Assess for malaria.
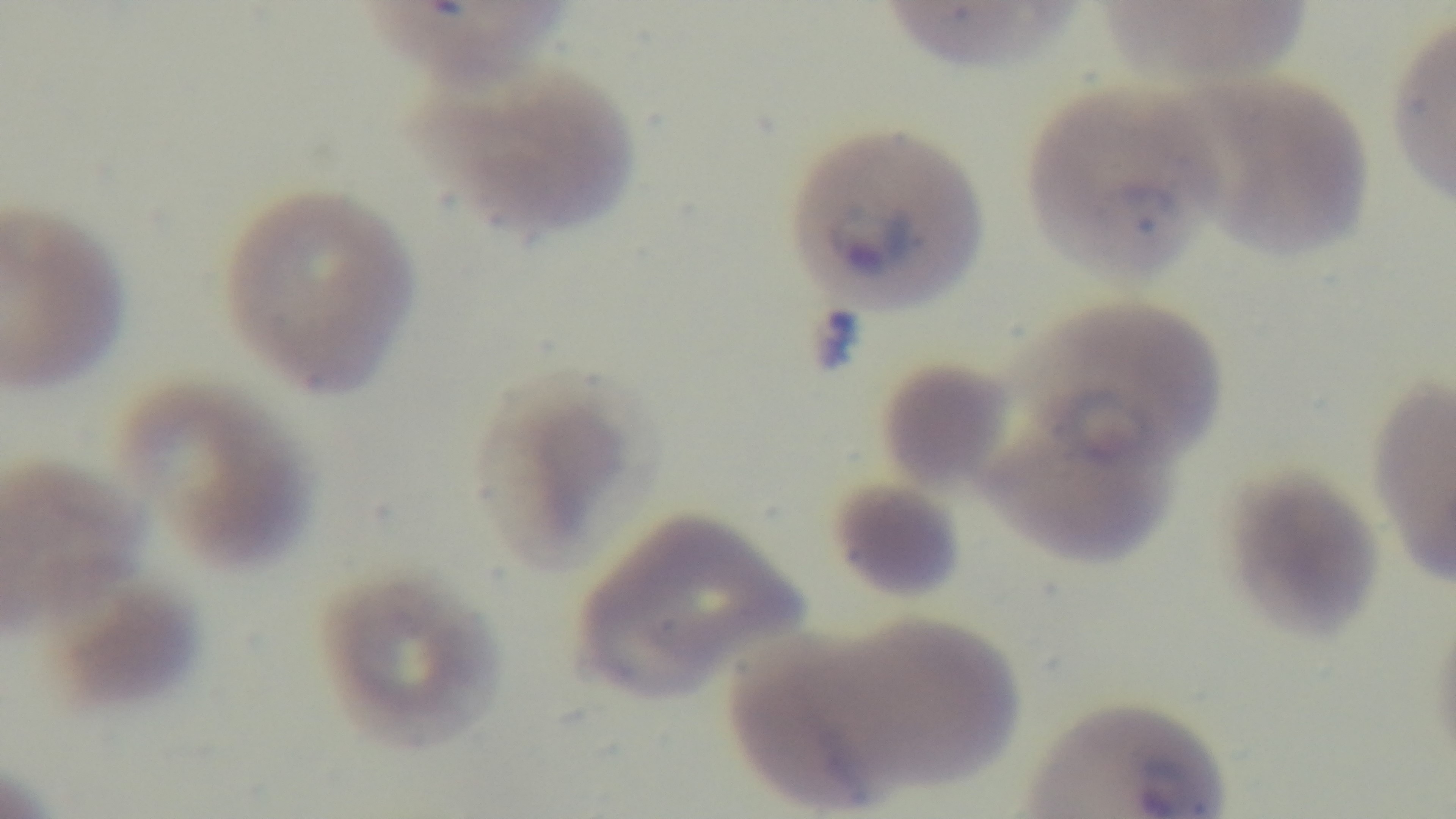
It is infected.

preparation: thin blood film
objective: 100x oil immersion
capture: mounted 4K digital camera
stain: Giemsa
modality: light microscopy
field_of_view: one from the slide